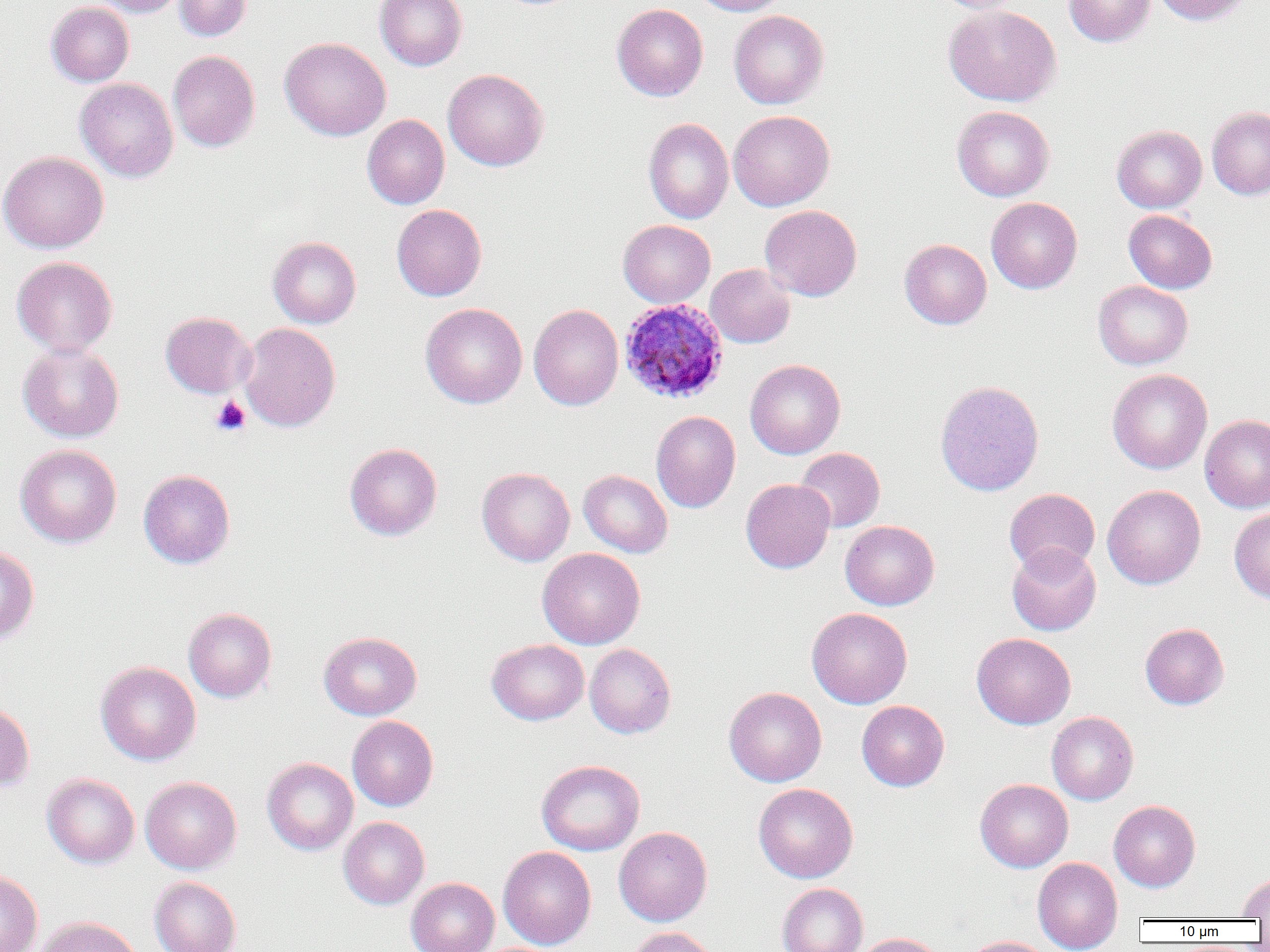

slide-level diagnosis = Plasmodium ovale
field of view = single
modality = optical microscopy
Plasmodium ovale-infected red blood cell locations = approximate bounding boxes as (x1, y1, x2, y2) in pixels: (619, 298, 728, 404)
image size = 1270×952 pixels
uninfected red blood cell locations = approximate bounding boxes as (x1, y1, x2, y2) in pixels: (91, 0, 187, 17), (174, 0, 251, 41), (375, 0, 467, 70), (691, 0, 789, 16), (931, 0, 1026, 13), (1064, 0, 1155, 46), (1152, 0, 1252, 26), (46, 1, 134, 86), (612, 3, 708, 101), (943, 4, 1061, 106), (729, 10, 829, 109), (280, 37, 391, 141), (168, 50, 260, 152), (442, 68, 549, 171), (75, 78, 178, 182), (952, 106, 1055, 201), (1207, 106, 1270, 200), (728, 110, 834, 211), (362, 115, 450, 209), (643, 118, 734, 224), (1111, 124, 1207, 212), (0, 151, 109, 253), (986, 197, 1082, 294), (392, 204, 486, 301), (760, 205, 862, 301), (1123, 209, 1217, 293), (618, 220, 715, 307), (268, 236, 361, 328), (899, 239, 992, 329), (11, 256, 118, 357), (705, 264, 795, 348), (1093, 280, 1193, 370), (420, 303, 527, 408), (529, 304, 624, 410), (160, 311, 255, 399), (239, 323, 340, 432), (18, 342, 124, 442), (745, 358, 845, 459), (1107, 368, 1212, 474), (935, 380, 1044, 497), (651, 411, 740, 513), (1200, 414, 1270, 513), (344, 442, 442, 541), (15, 444, 122, 548), (795, 447, 885, 532), (477, 467, 575, 566), (138, 469, 235, 569), (578, 469, 673, 557), (740, 479, 835, 573), (1102, 485, 1206, 589), (1004, 488, 1100, 576), (1229, 508, 1270, 603), (840, 520, 939, 610), (1007, 544, 1101, 636), (0, 546, 39, 644), (537, 547, 645, 649), (806, 607, 912, 709), (183, 608, 277, 702), (1140, 623, 1229, 710), (319, 631, 422, 720), (972, 632, 1076, 729), (487, 639, 589, 725), (585, 643, 676, 738), (95, 661, 201, 765), (724, 686, 827, 786), (857, 700, 949, 791), (0, 701, 34, 792), (1047, 712, 1138, 805), (347, 716, 438, 811), (262, 757, 358, 855), (536, 760, 645, 855), (42, 773, 139, 868), (140, 776, 242, 873), (975, 779, 1073, 872), (753, 783, 858, 883), (1108, 800, 1200, 892), (339, 816, 429, 909), (614, 826, 712, 926), (498, 846, 597, 949), (1033, 857, 1123, 952), (0, 869, 43, 952), (1236, 873, 1270, 919), (149, 876, 241, 952), (406, 877, 499, 952), (777, 883, 868, 952), (34, 916, 143, 952), (626, 926, 720, 952), (851, 933, 945, 952), (961, 936, 1054, 952)
magnification = 1000x
preparation = thin blood smear
platelet locations = approximate bounding boxes as (x1, y1, x2, y2) in pixels: (211, 396, 251, 436)